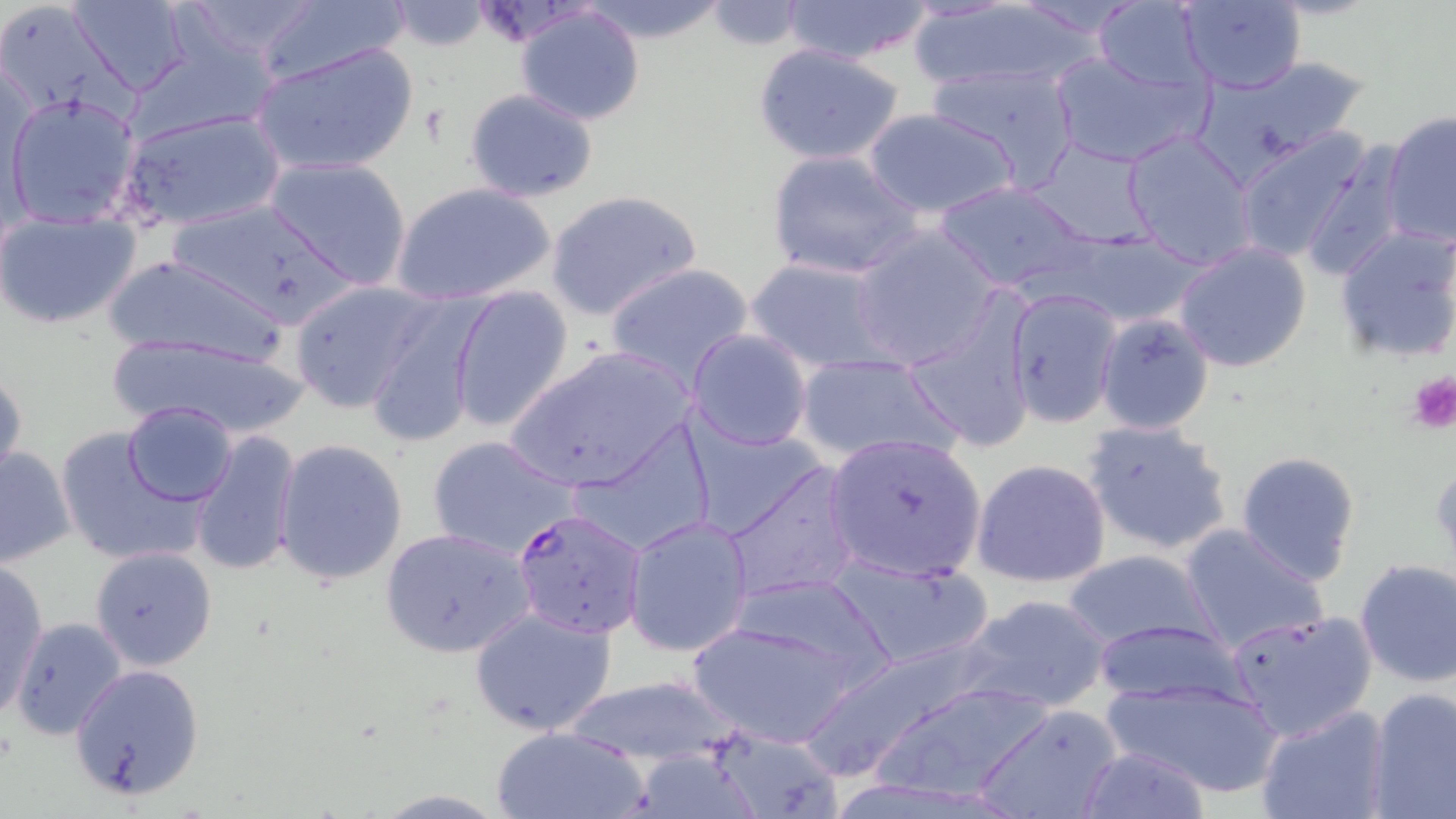

Approximate bounding boxes as [x1, y1, x2, y2] in pixels. Plasmodium falciparum-infected red blood cell locations: [513, 506, 647, 637]. Uninfected red blood cell locations: [67, 0, 194, 98], [169, 0, 328, 65], [575, 0, 732, 43], [782, 0, 932, 65], [1175, 0, 1305, 93], [251, 1, 415, 90], [1088, 1, 1210, 92], [385, 2, 494, 51], [701, 2, 808, 50], [908, 4, 1097, 91], [515, 5, 646, 126], [252, 41, 419, 175], [752, 43, 906, 166], [1048, 47, 1208, 169], [1200, 56, 1371, 169], [925, 63, 1079, 187], [465, 88, 600, 202], [4, 93, 141, 226], [862, 107, 1019, 219], [119, 108, 285, 231], [1383, 112, 1455, 248], [1122, 128, 1256, 267], [1233, 128, 1382, 268], [1026, 139, 1159, 248], [1300, 143, 1410, 282], [767, 148, 924, 281], [262, 156, 413, 289], [933, 180, 1094, 291], [391, 182, 558, 305], [546, 188, 701, 322], [163, 195, 358, 330], [1, 213, 142, 329], [1333, 224, 1456, 364], [1040, 225, 1210, 328], [848, 227, 1000, 370], [1172, 242, 1314, 373], [98, 253, 290, 367], [745, 257, 894, 373], [603, 261, 755, 392], [287, 280, 441, 414], [446, 284, 575, 433], [1005, 288, 1121, 428], [366, 296, 486, 450], [904, 301, 1037, 455], [1095, 312, 1215, 435], [687, 329, 812, 451], [107, 332, 310, 440], [503, 346, 698, 495], [794, 352, 960, 466], [0, 366, 26, 491], [121, 400, 237, 508], [684, 417, 825, 540], [1080, 418, 1235, 557], [563, 419, 718, 560], [55, 426, 209, 569], [188, 429, 304, 579], [822, 432, 988, 583], [427, 436, 578, 560], [274, 438, 408, 585], [0, 444, 77, 568], [1233, 451, 1362, 585], [971, 457, 1113, 589], [719, 458, 864, 605], [622, 514, 754, 657], [1177, 522, 1329, 654], [380, 527, 534, 658], [90, 546, 218, 671], [1060, 548, 1219, 654], [825, 552, 997, 672], [1353, 559, 1456, 687], [0, 560, 49, 723], [732, 572, 895, 687], [959, 593, 1113, 715], [469, 604, 617, 738], [1225, 608, 1377, 741], [8, 618, 127, 740], [687, 619, 865, 748], [1090, 619, 1251, 710], [800, 639, 994, 784], [66, 664, 204, 801], [559, 672, 740, 768], [1098, 673, 1286, 796], [863, 681, 1055, 804], [1367, 686, 1456, 819], [974, 704, 1123, 819], [1255, 704, 1391, 819], [702, 724, 845, 819], [491, 726, 650, 819], [1076, 744, 1211, 819], [620, 747, 772, 819]. Platelet locations: [1404, 370, 1456, 435]. Slide-level diagnosis: Plasmodium falciparum. Light microscopy. May-Grünwald-Giemsa-stained preparation. Thin blood smear. Image is 1456×819 pixels. Captured at 1000x magnification. One field of a larger specimen.